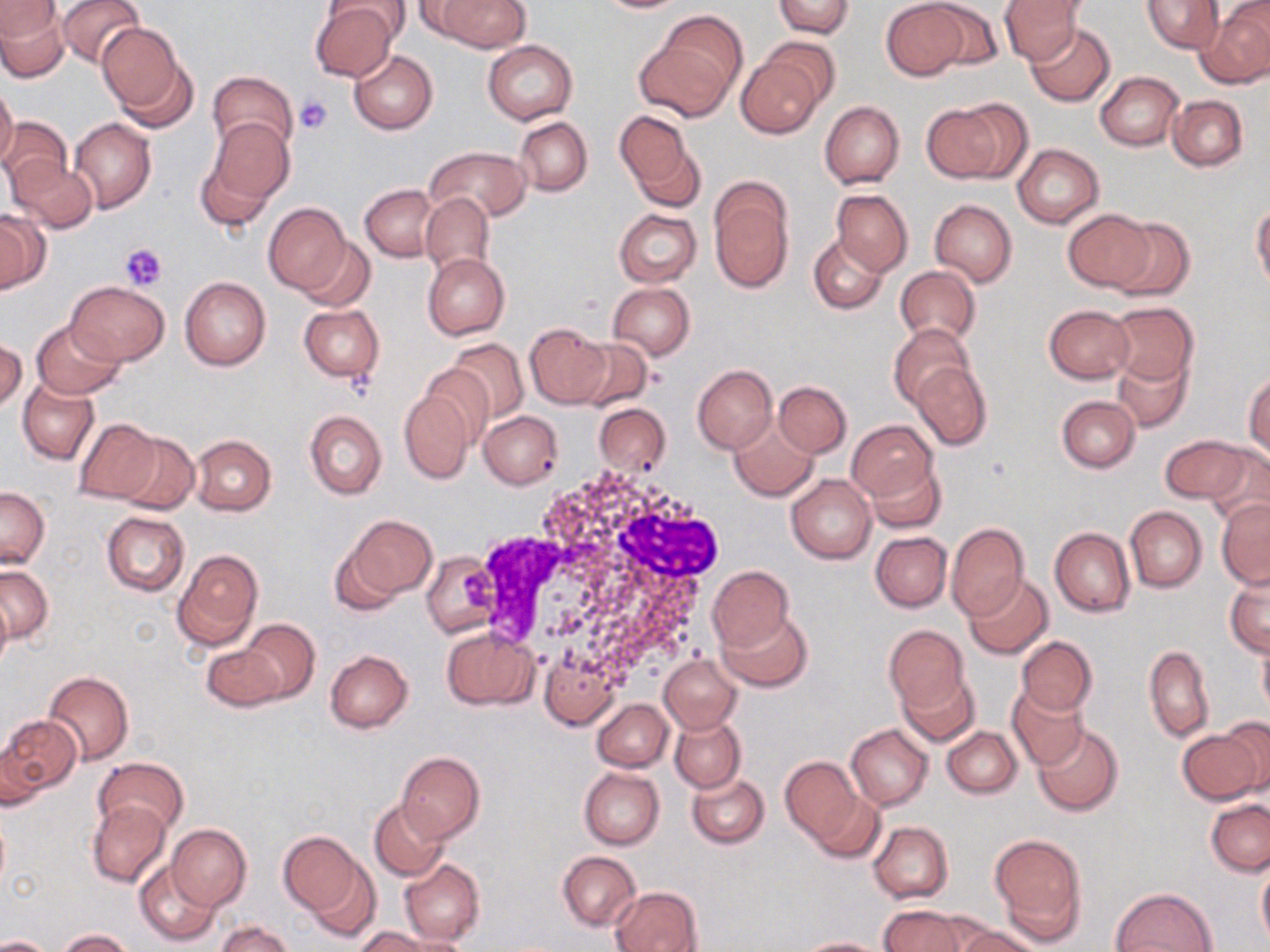 Approximate bounding boxes as named x1/y1/x2/y2 corners in pixels. Platelet locations: (x1=295, y1=96, x2=334, y2=134), (x1=121, y1=242, x2=169, y2=289). Uninfected red blood cell locations: (x1=55, y1=0, x2=144, y2=68), (x1=408, y1=0, x2=487, y2=38), (x1=434, y1=0, x2=531, y2=52), (x1=594, y1=0, x2=688, y2=13), (x1=881, y1=0, x2=969, y2=80), (x1=920, y1=0, x2=1006, y2=71), (x1=999, y1=0, x2=1083, y2=64), (x1=1142, y1=0, x2=1223, y2=54), (x1=0, y1=1, x2=59, y2=38), (x1=772, y1=1, x2=854, y2=37), (x1=309, y1=2, x2=401, y2=83), (x1=0, y1=5, x2=69, y2=81), (x1=1199, y1=5, x2=1270, y2=88), (x1=96, y1=22, x2=189, y2=120), (x1=1027, y1=22, x2=1116, y2=104), (x1=635, y1=31, x2=738, y2=120), (x1=759, y1=38, x2=840, y2=111), (x1=483, y1=40, x2=578, y2=124), (x1=349, y1=50, x2=437, y2=133), (x1=736, y1=52, x2=826, y2=138), (x1=207, y1=70, x2=298, y2=155), (x1=1095, y1=71, x2=1184, y2=151), (x1=0, y1=83, x2=19, y2=170), (x1=1168, y1=95, x2=1247, y2=171), (x1=819, y1=101, x2=904, y2=188), (x1=922, y1=103, x2=1005, y2=183), (x1=613, y1=111, x2=694, y2=194), (x1=0, y1=116, x2=72, y2=196), (x1=70, y1=117, x2=157, y2=212), (x1=514, y1=117, x2=592, y2=196), (x1=207, y1=118, x2=294, y2=208), (x1=631, y1=141, x2=706, y2=214), (x1=1012, y1=144, x2=1103, y2=228), (x1=425, y1=147, x2=531, y2=223), (x1=194, y1=154, x2=275, y2=234), (x1=10, y1=159, x2=98, y2=232), (x1=710, y1=182, x2=795, y2=292), (x1=360, y1=184, x2=440, y2=261), (x1=831, y1=189, x2=913, y2=277), (x1=420, y1=193, x2=493, y2=274), (x1=929, y1=199, x2=1016, y2=287), (x1=1252, y1=201, x2=1270, y2=292), (x1=263, y1=204, x2=351, y2=296), (x1=614, y1=208, x2=701, y2=287), (x1=1064, y1=209, x2=1154, y2=294), (x1=0, y1=210, x2=49, y2=291), (x1=1107, y1=216, x2=1195, y2=303), (x1=808, y1=235, x2=888, y2=314), (x1=299, y1=237, x2=373, y2=311), (x1=422, y1=253, x2=510, y2=340), (x1=895, y1=265, x2=981, y2=348), (x1=179, y1=276, x2=271, y2=371), (x1=66, y1=281, x2=169, y2=365), (x1=608, y1=281, x2=696, y2=359), (x1=1107, y1=303, x2=1197, y2=388), (x1=298, y1=304, x2=384, y2=382), (x1=1044, y1=305, x2=1134, y2=383), (x1=31, y1=318, x2=126, y2=401), (x1=525, y1=324, x2=610, y2=408), (x1=889, y1=324, x2=974, y2=410), (x1=571, y1=337, x2=652, y2=410), (x1=0, y1=338, x2=26, y2=413), (x1=446, y1=339, x2=530, y2=425), (x1=1113, y1=351, x2=1192, y2=433), (x1=418, y1=361, x2=496, y2=447), (x1=911, y1=361, x2=992, y2=452), (x1=692, y1=365, x2=776, y2=452), (x1=1069, y1=366, x2=1188, y2=456), (x1=1245, y1=370, x2=1270, y2=458), (x1=19, y1=378, x2=100, y2=465), (x1=774, y1=380, x2=851, y2=456), (x1=397, y1=389, x2=476, y2=484), (x1=1057, y1=396, x2=1140, y2=472), (x1=593, y1=403, x2=672, y2=476), (x1=304, y1=410, x2=386, y2=500), (x1=480, y1=410, x2=562, y2=489), (x1=73, y1=418, x2=162, y2=505), (x1=729, y1=418, x2=818, y2=501), (x1=847, y1=422, x2=935, y2=501), (x1=115, y1=432, x2=199, y2=516), (x1=190, y1=435, x2=276, y2=515), (x1=1160, y1=435, x2=1256, y2=506), (x1=1200, y1=443, x2=1270, y2=523), (x1=868, y1=460, x2=946, y2=533), (x1=786, y1=474, x2=876, y2=563), (x1=0, y1=488, x2=50, y2=568), (x1=1216, y1=499, x2=1270, y2=588), (x1=1125, y1=506, x2=1207, y2=592), (x1=102, y1=512, x2=189, y2=596), (x1=347, y1=514, x2=436, y2=601), (x1=946, y1=523, x2=1029, y2=619), (x1=1049, y1=526, x2=1135, y2=617), (x1=870, y1=532, x2=952, y2=612), (x1=330, y1=542, x2=403, y2=618), (x1=172, y1=549, x2=262, y2=653), (x1=423, y1=550, x2=501, y2=639), (x1=0, y1=565, x2=53, y2=644), (x1=707, y1=565, x2=794, y2=651), (x1=1225, y1=569, x2=1270, y2=658), (x1=965, y1=574, x2=1053, y2=659), (x1=0, y1=588, x2=13, y2=672), (x1=718, y1=610, x2=812, y2=693), (x1=239, y1=619, x2=319, y2=704), (x1=884, y1=625, x2=968, y2=713), (x1=443, y1=627, x2=536, y2=708), (x1=1017, y1=636, x2=1096, y2=718), (x1=1258, y1=638, x2=1270, y2=723), (x1=202, y1=643, x2=285, y2=712), (x1=1144, y1=646, x2=1215, y2=743), (x1=326, y1=651, x2=412, y2=733), (x1=660, y1=653, x2=741, y2=734), (x1=897, y1=670, x2=979, y2=748), (x1=43, y1=672, x2=133, y2=765), (x1=1009, y1=686, x2=1089, y2=770), (x1=592, y1=699, x2=673, y2=771), (x1=670, y1=714, x2=745, y2=792), (x1=3, y1=717, x2=82, y2=798), (x1=1220, y1=718, x2=1270, y2=798), (x1=847, y1=724, x2=932, y2=810), (x1=1033, y1=725, x2=1124, y2=817), (x1=942, y1=727, x2=1021, y2=798), (x1=1177, y1=729, x2=1264, y2=805), (x1=1, y1=744, x2=46, y2=811), (x1=396, y1=751, x2=485, y2=844), (x1=95, y1=756, x2=188, y2=837), (x1=780, y1=756, x2=861, y2=843), (x1=579, y1=767, x2=665, y2=849), (x1=687, y1=774, x2=769, y2=849), (x1=811, y1=790, x2=884, y2=863), (x1=1206, y1=797, x2=1270, y2=876), (x1=370, y1=799, x2=450, y2=882), (x1=88, y1=800, x2=171, y2=888), (x1=869, y1=821, x2=953, y2=902), (x1=167, y1=825, x2=251, y2=911), (x1=278, y1=833, x2=364, y2=916), (x1=989, y1=834, x2=1087, y2=940), (x1=558, y1=851, x2=642, y2=932), (x1=304, y1=856, x2=381, y2=943), (x1=399, y1=858, x2=483, y2=947), (x1=1257, y1=858, x2=1270, y2=950), (x1=135, y1=859, x2=221, y2=946), (x1=611, y1=886, x2=702, y2=952), (x1=1111, y1=887, x2=1218, y2=952), (x1=878, y1=905, x2=969, y2=952), (x1=216, y1=921, x2=293, y2=951), (x1=357, y1=924, x2=456, y2=952), (x1=954, y1=926, x2=1042, y2=952), (x1=59, y1=929, x2=135, y2=951), (x1=1, y1=934, x2=53, y2=951), (x1=797, y1=937, x2=889, y2=951). White blood cell locations: (x1=462, y1=466, x2=725, y2=692). Slide-level diagnosis: negative for blood parasites. Single field of view. Thin blood smear. Image is 1270×952 pixels. May-Grünwald-Giemsa stain. 1000x magnification. Optical microscopy.